Locate every Plasmodium vivax-infected red blood cell.
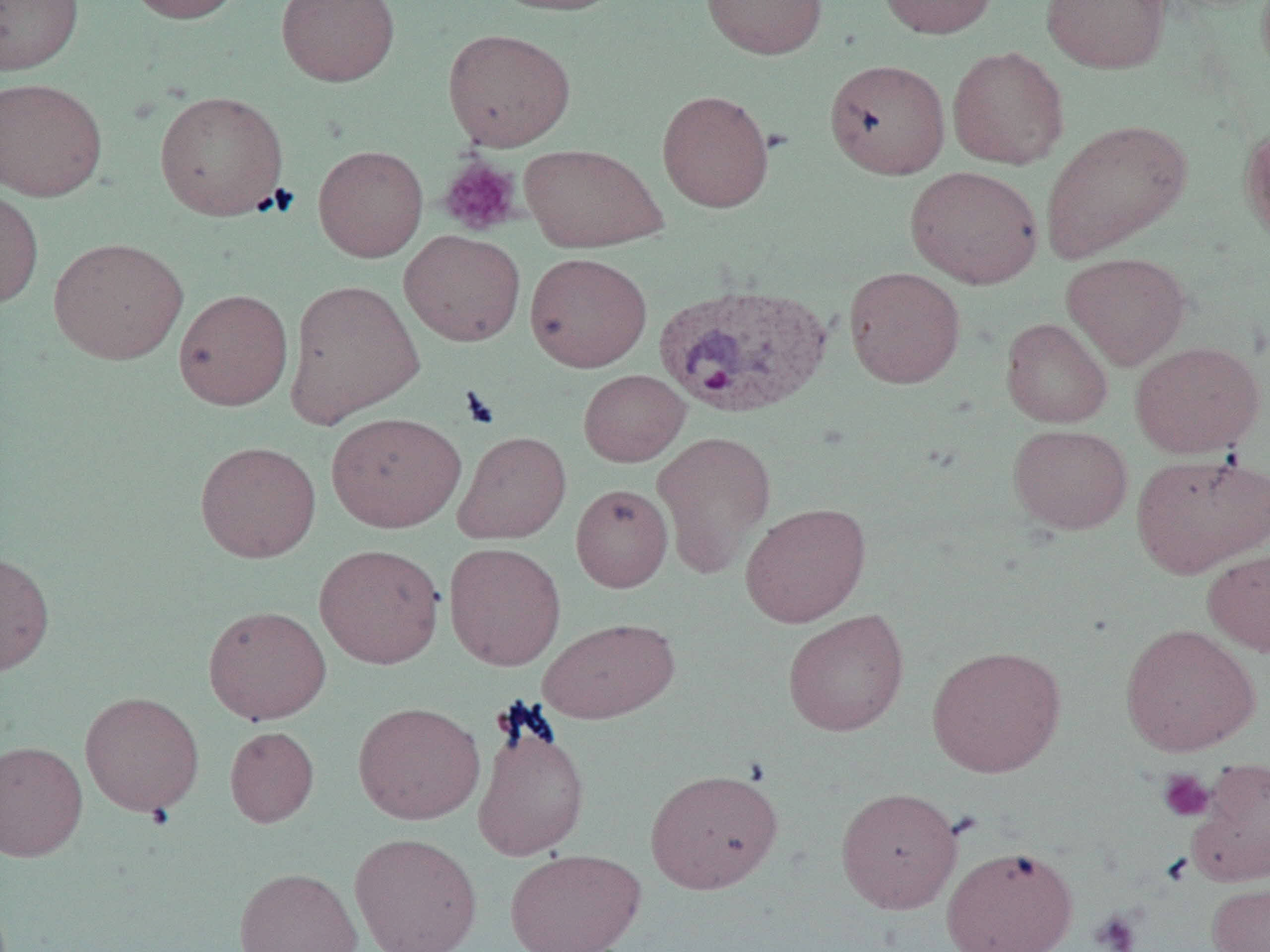

Approximate bounding boxes as (x1,y1)-(x2,y2) corner pairs in pixels.
Plasmodium vivax-infected red blood cells: (654,282)-(832,419).

{
  "slide_level_diagnosis": "Plasmodium vivax",
  "platelet_locations": "approximate bounding boxes as (x1,y1)-(x2,y2) corner pairs in pixels: (438,157)-(522,236), (1157,768)-(1215,822), (1090,910)-(1142,952)",
  "preparation": "thin blood film",
  "image_size": "1270×952 pixels",
  "modality": "optical microscopy",
  "uninfected_red_blood_cell_locations": "approximate bounding boxes as (x1,y1)-(x2,y2) corner pairs in pixels: (0,0)-(83,75), (126,0)-(247,24), (276,0)-(400,87), (489,0)-(629,16), (701,0)-(828,60), (877,0)-(999,38), (1041,0)-(1171,74), (443,28)-(575,151), (947,45)-(1069,169), (824,59)-(951,179), (0,77)-(107,201), (657,89)-(775,212), (154,90)-(289,221), (1040,120)-(1191,262), (1239,122)-(1270,246), (519,143)-(668,252), (313,144)-(428,262), (906,165)-(1043,288), (0,187)-(44,308), (399,229)-(526,346), (48,237)-(188,364), (525,252)-(652,372), (1062,252)-(1190,370), (843,266)-(966,389), (284,278)-(425,427), (173,288)-(293,411), (1000,318)-(1112,427), (1130,341)-(1264,459), (579,369)-(690,467), (326,411)-(466,533), (1008,424)-(1132,534), (453,431)-(572,544), (652,431)-(776,579), (195,440)-(321,563), (1131,451)-(1270,578), (571,483)-(673,593), (740,502)-(871,627), (444,542)-(566,671), (314,543)-(444,669), (1202,549)-(1270,656), (0,551)-(55,676), (203,605)-(331,724), (783,608)-(909,737), (537,617)-(679,724), (1120,623)-(1260,756), (927,644)-(1066,778), (80,691)-(204,816), (352,701)-(485,825), (471,714)-(590,863), (225,726)-(319,827), (0,740)-(87,861), (1188,756)-(1270,885), (645,768)-(783,894), (836,787)-(962,914), (349,831)-(483,952), (941,845)-(1078,952), (505,847)-(645,952), (233,866)-(363,952), (1206,879)-(1270,952)",
  "field_of_view": "single",
  "magnification": "1000x"
}